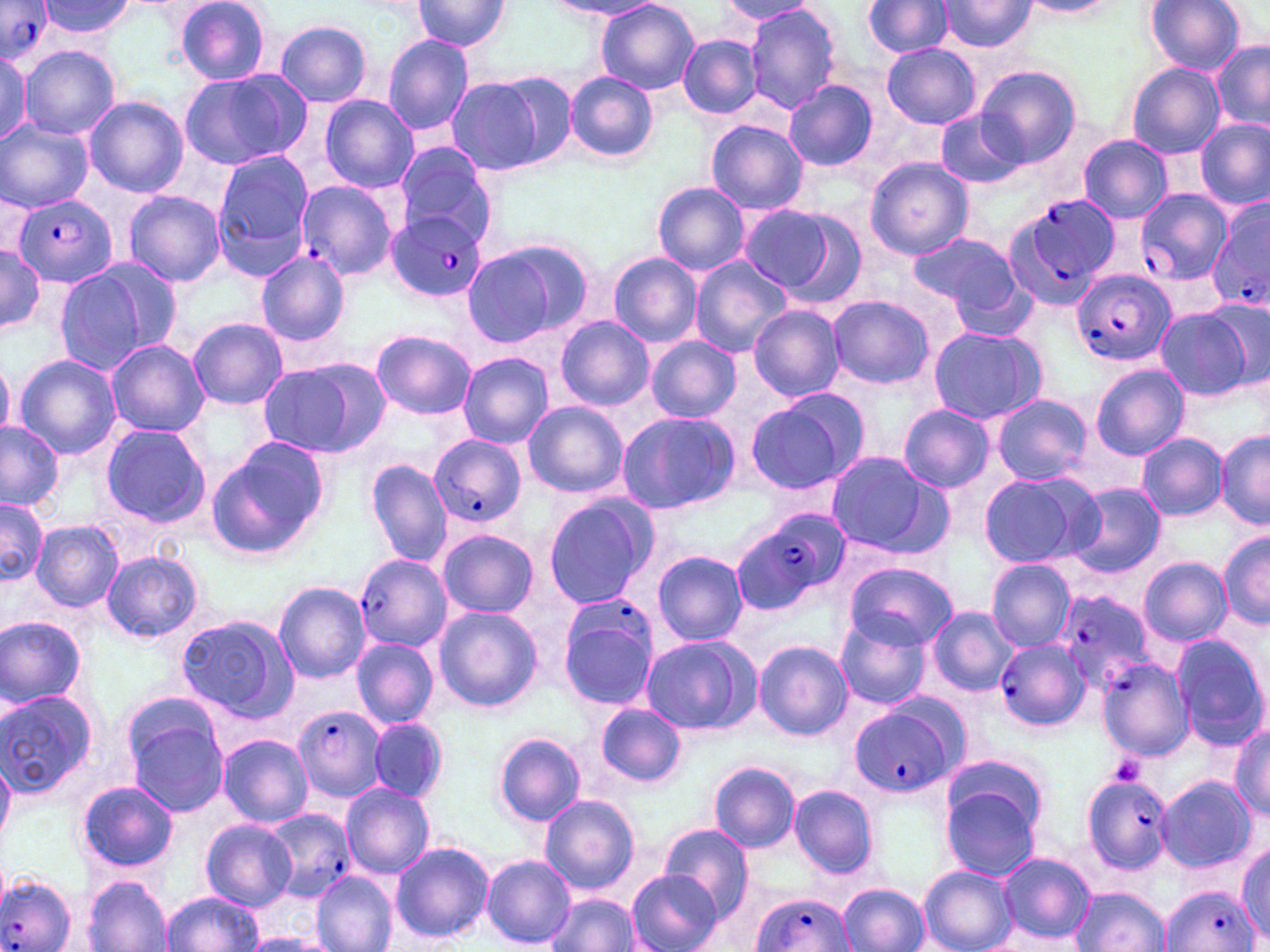
Approximate bounding boxes as (x1, y1, x2, y2) in pixels. Uninfected red blood cell locations: (37, 0, 136, 39), (412, 0, 510, 53), (175, 1, 274, 84), (550, 1, 668, 20), (596, 1, 700, 94), (719, 1, 822, 25), (936, 1, 1039, 54), (1018, 1, 1124, 19), (1145, 1, 1246, 76), (862, 2, 955, 58), (744, 3, 840, 115), (275, 19, 372, 107), (382, 34, 474, 138), (679, 34, 762, 120), (1211, 41, 1270, 131), (881, 43, 981, 128), (21, 46, 121, 139), (0, 50, 32, 145), (1126, 61, 1226, 158), (977, 66, 1079, 167), (178, 70, 307, 168), (452, 70, 577, 175), (565, 71, 659, 163), (784, 79, 879, 172), (319, 94, 418, 193), (84, 96, 188, 198), (934, 109, 1026, 190), (1197, 118, 1269, 211), (706, 119, 807, 215), (0, 120, 93, 211), (1077, 134, 1173, 223), (392, 145, 499, 248), (212, 150, 316, 278), (866, 158, 974, 260), (651, 182, 751, 276), (123, 190, 226, 287), (737, 204, 843, 294), (908, 231, 1023, 318), (461, 240, 590, 349), (0, 244, 46, 336), (255, 250, 349, 347), (608, 252, 702, 347), (689, 253, 794, 357), (54, 261, 164, 376), (828, 295, 935, 390), (1194, 299, 1268, 390), (748, 304, 846, 401), (1153, 306, 1253, 401), (555, 315, 654, 411), (188, 317, 288, 409), (926, 325, 1047, 424), (370, 329, 476, 420), (645, 336, 741, 422), (104, 339, 210, 438), (457, 351, 553, 449), (14, 355, 122, 460), (259, 357, 390, 458), (1090, 363, 1190, 461), (746, 389, 868, 494), (990, 393, 1091, 485), (522, 401, 629, 499), (898, 406, 994, 491), (614, 410, 740, 516), (0, 421, 65, 510), (99, 423, 211, 526), (1216, 431, 1270, 529), (1137, 432, 1227, 522), (206, 439, 329, 560), (823, 450, 946, 556), (366, 457, 453, 568), (977, 470, 1099, 569), (1068, 482, 1166, 578), (540, 493, 656, 611), (0, 500, 46, 586), (30, 521, 123, 610), (436, 529, 538, 618), (1220, 529, 1269, 630), (652, 549, 749, 646), (100, 551, 202, 642), (1138, 557, 1232, 646), (987, 559, 1076, 650), (841, 560, 956, 651), (273, 583, 373, 684), (433, 605, 542, 713), (927, 606, 1018, 696), (175, 613, 297, 722), (0, 615, 89, 708), (835, 618, 929, 710), (638, 633, 762, 737), (1170, 633, 1267, 752), (351, 636, 439, 728), (754, 640, 851, 740), (1097, 658, 1194, 761), (1, 688, 100, 796), (595, 703, 686, 787), (125, 709, 230, 819), (369, 717, 449, 803), (1230, 724, 1270, 820), (493, 731, 586, 827), (218, 734, 313, 827), (942, 753, 1052, 838), (708, 760, 800, 851), (1155, 776, 1257, 872), (938, 778, 1044, 882), (77, 780, 180, 873), (342, 782, 436, 879), (789, 786, 879, 878), (538, 793, 640, 895), (200, 820, 296, 911), (658, 823, 756, 916), (389, 840, 495, 945), (1236, 842, 1269, 946), (996, 850, 1095, 944), (481, 855, 576, 948), (919, 866, 1017, 952), (311, 871, 397, 952), (626, 871, 720, 952), (85, 876, 173, 951), (839, 883, 929, 952), (1069, 888, 1172, 952), (160, 891, 263, 951), (548, 893, 641, 951), (239, 933, 333, 951). Plasmodium falciparum-infected red blood cell locations: (0, 1, 58, 66), (294, 179, 398, 282), (1135, 188, 1232, 288), (13, 193, 117, 289), (1008, 194, 1117, 303), (1206, 195, 1270, 315), (388, 209, 488, 303), (1073, 270, 1174, 368), (430, 435, 528, 527), (729, 508, 848, 617), (355, 555, 450, 652), (1054, 592, 1156, 692), (556, 595, 660, 709), (994, 637, 1090, 732), (849, 699, 963, 799), (292, 702, 387, 800), (1079, 777, 1174, 883), (261, 809, 354, 902), (1, 873, 77, 952), (1162, 885, 1261, 952), (750, 893, 854, 952). Platelet locations: (1109, 753, 1147, 784). Slide-level diagnosis: Plasmodium falciparum. Single field of view. Optical microscopy. May-Grünwald-Giemsa stain. Captured at 1000x magnification. Thin blood film. Image is 1270×952 pixels.